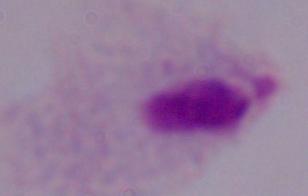

A trichomonad is seen. Micrograph. 1000x magnification.